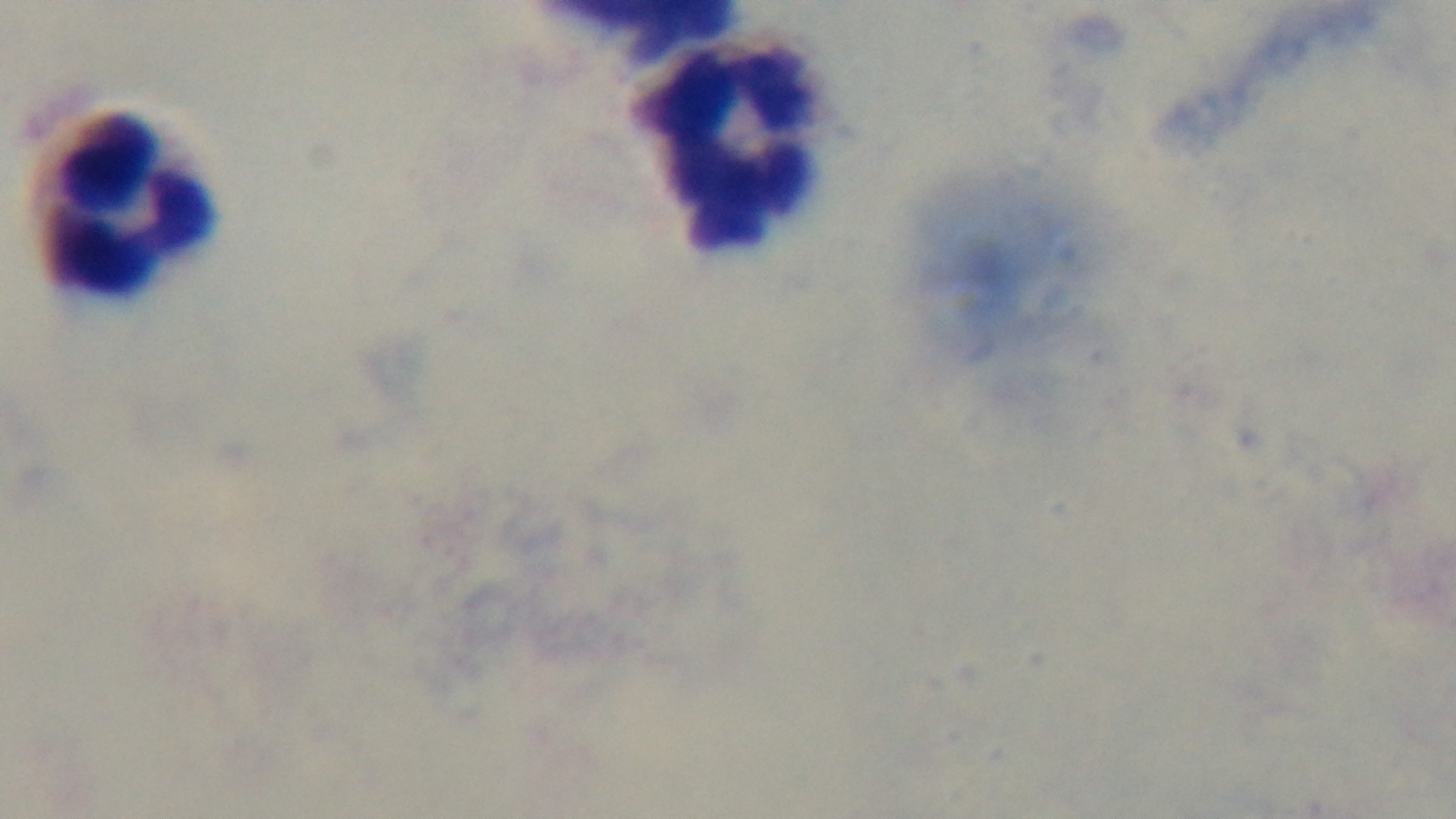
Captured with a mounted 4K digital camera. Giemsa-stained. 100x oil-immersion objective. One field from the slide. Malaria status: negative. Photomicrograph. Preparation: thick smear.